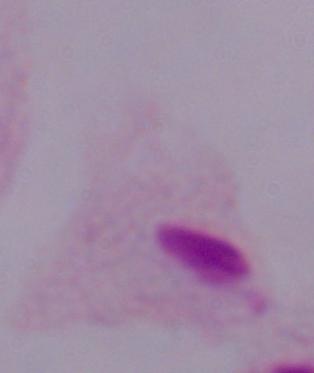
Summary:
  - Magnification: 1000x
  - Identification: trichomonad
  - Modality: photomicrograph